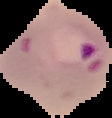
image type = cell region segmented out of the field of view; surrounding area masked to black
image size = 112×118 pixels
preparation = thin blood smear
result = malaria parasites identified